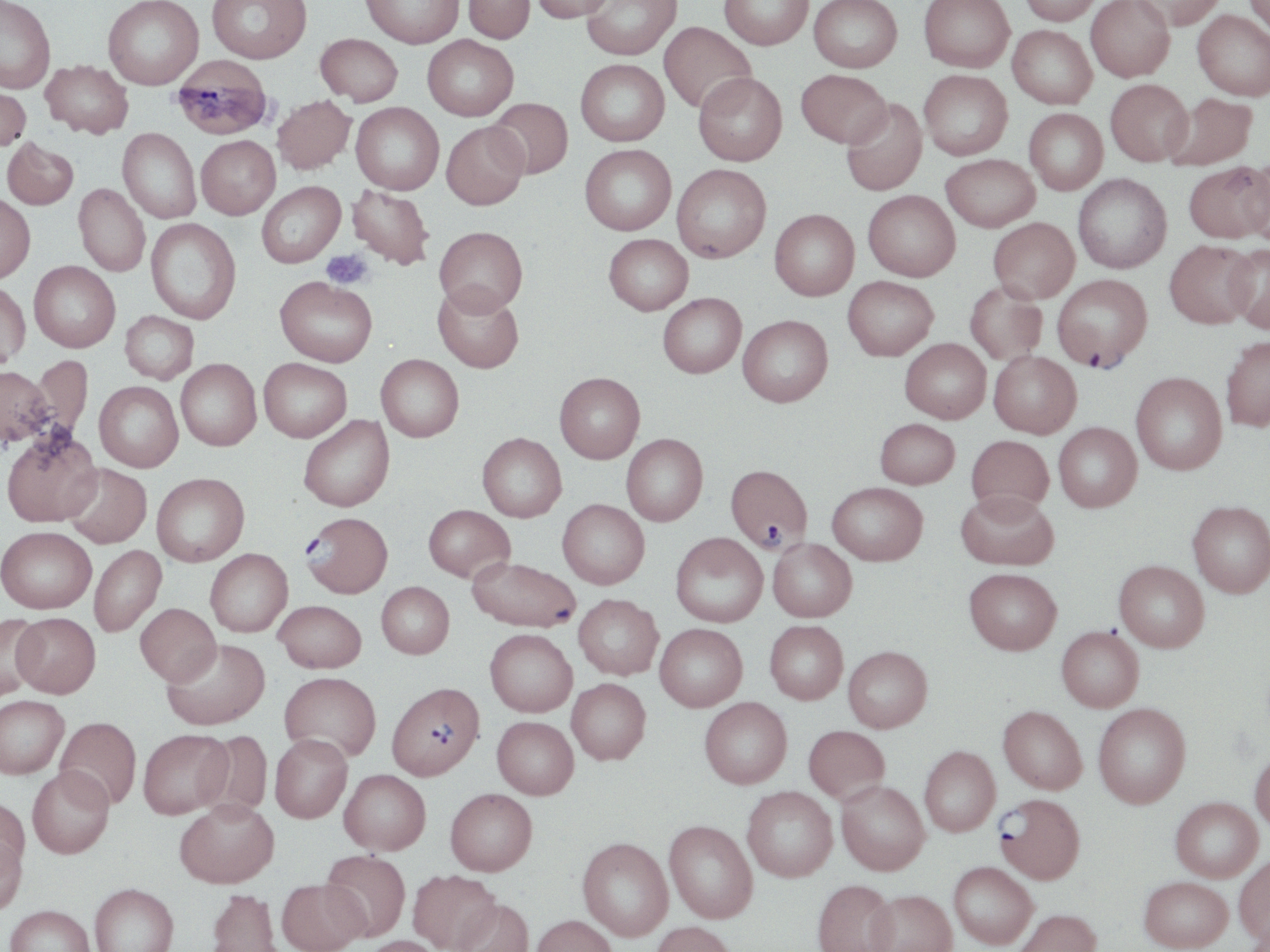 Approximate bounding boxes as [x1, y1, x2, y2] in pixels. Plasmodium falciparum-infected red blood cell locations: [1053, 274, 1152, 372], [724, 463, 814, 552], [301, 511, 394, 597], [386, 682, 484, 781], [995, 793, 1086, 884]. Uninfected red blood cell locations: [102, 0, 203, 89], [207, 0, 312, 63], [362, 0, 463, 48], [463, 0, 534, 43], [530, 0, 616, 21], [581, 0, 681, 60], [720, 0, 812, 50], [809, 0, 902, 73], [919, 0, 1015, 72], [1018, 0, 1102, 25], [1086, 0, 1175, 82], [1130, 0, 1225, 30], [1243, 0, 1270, 42], [0, 1, 56, 93], [1192, 10, 1270, 101], [659, 22, 756, 113], [1007, 25, 1097, 109], [315, 33, 403, 106], [422, 35, 519, 121], [171, 55, 274, 140], [575, 59, 669, 146], [41, 60, 133, 138], [796, 69, 891, 148], [919, 69, 1012, 160], [693, 72, 788, 166], [1105, 79, 1192, 165], [0, 80, 31, 151], [1163, 92, 1258, 170], [272, 95, 355, 174], [487, 97, 573, 179], [841, 98, 927, 196], [351, 102, 444, 194], [1024, 108, 1108, 195], [441, 121, 529, 210], [117, 129, 201, 223], [196, 135, 280, 219], [2, 137, 78, 210], [580, 144, 676, 235], [941, 153, 1040, 231], [1242, 156, 1270, 246], [1185, 162, 1270, 243], [672, 164, 771, 262], [1073, 174, 1172, 274], [256, 181, 345, 268], [74, 183, 150, 276], [347, 185, 434, 269], [863, 190, 959, 281], [0, 193, 35, 282], [770, 209, 859, 300], [988, 217, 1079, 303], [146, 218, 241, 324], [434, 226, 527, 315], [603, 233, 693, 315], [1164, 239, 1259, 328], [1223, 242, 1270, 333], [29, 261, 120, 352], [843, 275, 938, 360], [275, 277, 377, 366], [0, 281, 30, 369], [964, 282, 1048, 365], [432, 283, 524, 373], [658, 293, 746, 377], [120, 311, 199, 383], [738, 315, 833, 407], [1221, 335, 1270, 432], [900, 338, 990, 423], [989, 351, 1081, 438], [376, 354, 464, 442], [29, 355, 94, 442], [175, 358, 261, 450], [259, 358, 352, 442], [0, 365, 53, 447], [554, 372, 644, 463], [1130, 372, 1227, 475], [94, 381, 183, 472], [299, 415, 394, 511], [875, 418, 960, 489], [1053, 422, 1142, 512], [1, 428, 102, 526], [477, 432, 566, 522], [621, 434, 708, 525], [966, 435, 1054, 515], [63, 463, 151, 548], [151, 473, 249, 566], [827, 482, 928, 565], [956, 490, 1058, 570], [557, 499, 649, 589], [1188, 500, 1270, 597], [423, 504, 515, 582], [0, 525, 96, 613], [670, 532, 768, 627], [768, 538, 857, 621], [89, 545, 166, 637], [205, 548, 293, 636], [467, 557, 578, 632], [1114, 560, 1209, 652], [964, 568, 1062, 654], [376, 581, 454, 658], [574, 594, 663, 679], [274, 599, 366, 673], [135, 604, 221, 685], [0, 613, 46, 700], [12, 613, 100, 697], [764, 620, 848, 704], [655, 623, 748, 711], [1057, 626, 1144, 712], [485, 628, 577, 716], [162, 638, 270, 730], [843, 646, 932, 732], [280, 671, 381, 762], [567, 678, 651, 764], [0, 695, 69, 778], [699, 697, 792, 788], [1093, 702, 1191, 808], [998, 706, 1087, 794], [55, 716, 142, 809], [492, 716, 579, 799], [803, 725, 889, 803], [138, 729, 232, 819], [197, 729, 273, 819], [270, 734, 352, 823], [919, 746, 1000, 836], [1250, 748, 1270, 832], [27, 766, 115, 858], [340, 769, 431, 854], [837, 781, 929, 875], [742, 786, 837, 882], [445, 788, 537, 875], [0, 795, 30, 879], [1170, 797, 1262, 882], [175, 799, 278, 888], [664, 820, 758, 923], [0, 830, 28, 916], [577, 837, 673, 941], [321, 849, 411, 941], [1234, 855, 1270, 946], [949, 861, 1037, 949], [408, 869, 501, 952], [1139, 875, 1232, 951], [277, 878, 367, 952], [812, 879, 897, 952], [89, 882, 179, 952], [206, 888, 283, 952], [867, 889, 957, 952], [453, 898, 534, 952], [4, 904, 95, 952], [1013, 909, 1101, 952], [532, 914, 617, 952], [650, 921, 737, 952], [362, 935, 445, 952]. Platelet locations: [321, 249, 373, 289]. Slide-level diagnosis: Plasmodium falciparum. May-Grünwald-Giemsa stain. Thin blood smear. Image is 1270×952 pixels. Single field of view. Captured at 1000x magnification. Light microscopy.